Evaluate for malaria.
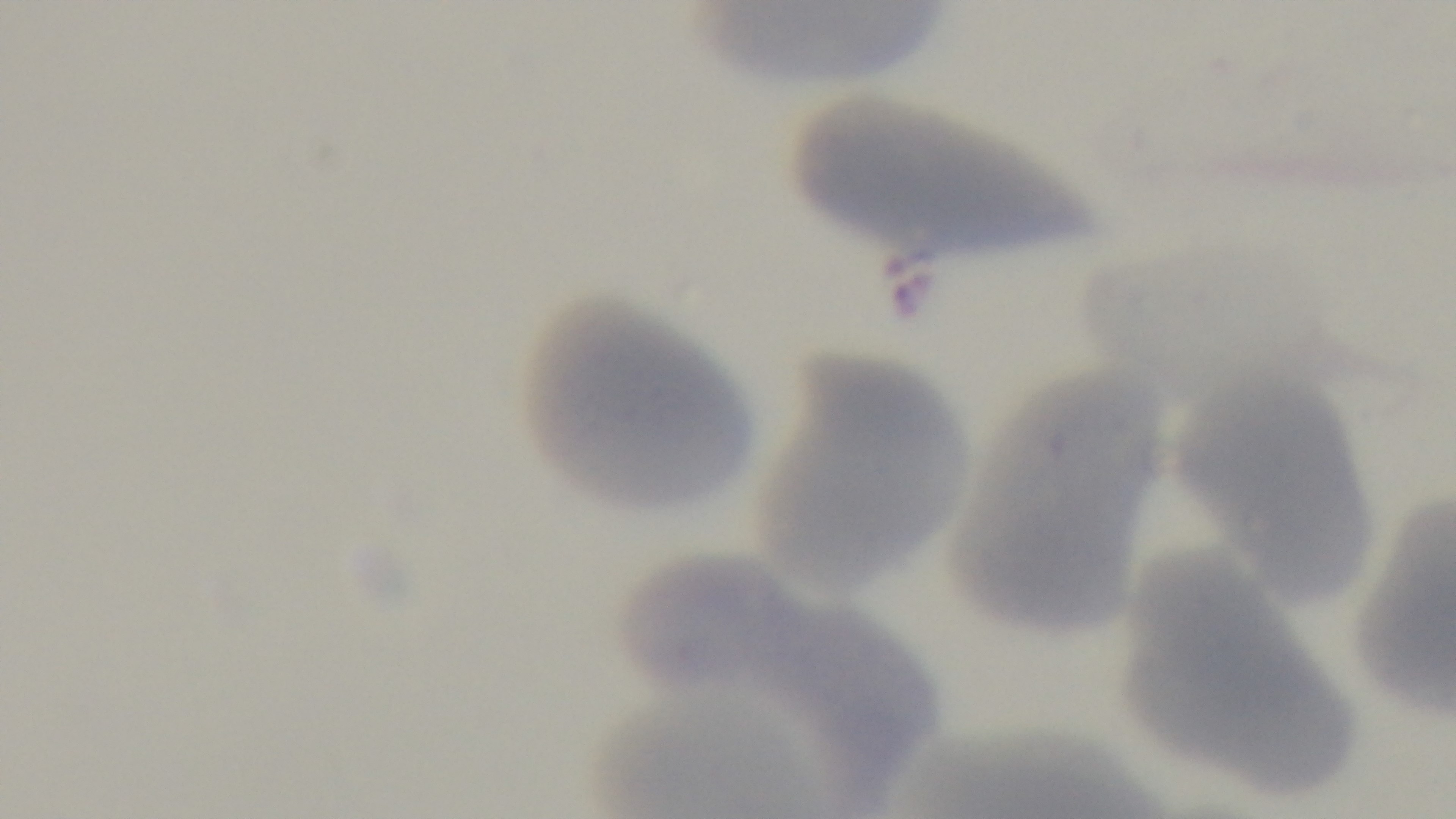

It is uninfected.

capture: mounted 4K digital camera
field_of_view: one from the slide
objective: 100x oil immersion
stain: Giemsa
preparation: thin
modality: light microscopy